Outline each blood parasite and name the species.
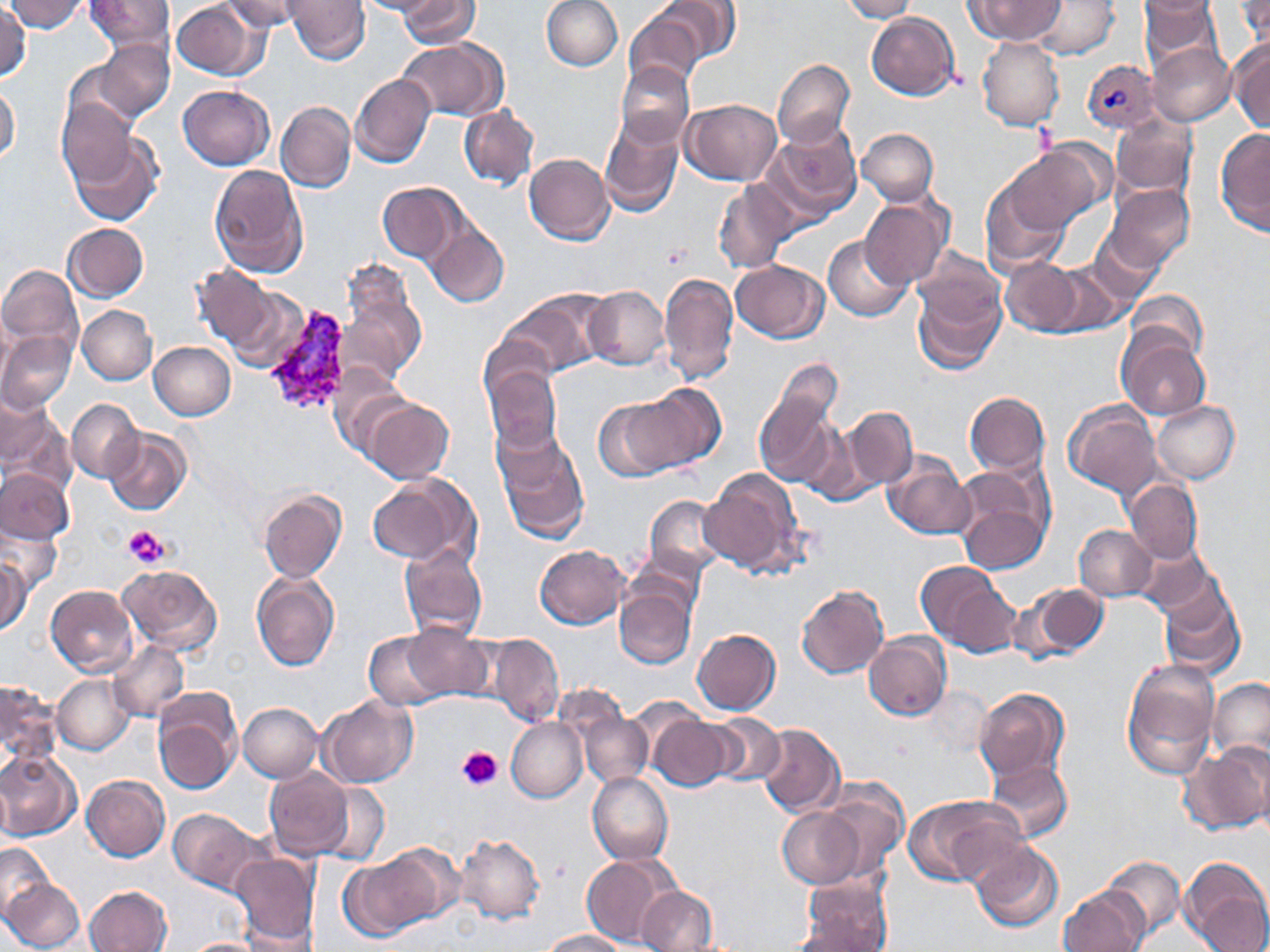
Approximate bounding boxes as named x1/y1/x2/y2 corners in pixels.
Plasmodium vivax-infected red blood cells: (x1=1082, y1=59, x2=1161, y2=133), (x1=261, y1=302, x2=355, y2=417).
No Plasmodium falciparum, Plasmodium ovale, Plasmodium malariae, Babesia divergens, or Trypanosoma brucei observed.

Summary:
  - Uninfected red blood cell locations: (x1=5, y1=0, x2=88, y2=32), (x1=86, y1=0, x2=173, y2=55), (x1=220, y1=0, x2=303, y2=32), (x1=285, y1=0, x2=370, y2=64), (x1=356, y1=0, x2=449, y2=18), (x1=399, y1=0, x2=478, y2=47), (x1=541, y1=0, x2=621, y2=70), (x1=655, y1=0, x2=739, y2=65), (x1=840, y1=0, x2=917, y2=22), (x1=966, y1=0, x2=1066, y2=45), (x1=1028, y1=0, x2=1119, y2=60), (x1=1139, y1=0, x2=1222, y2=71), (x1=1234, y1=0, x2=1270, y2=45), (x1=172, y1=1, x2=264, y2=79), (x1=0, y1=6, x2=30, y2=80), (x1=624, y1=11, x2=706, y2=90), (x1=866, y1=12, x2=959, y2=101), (x1=396, y1=38, x2=507, y2=120), (x1=978, y1=38, x2=1064, y2=130), (x1=92, y1=40, x2=175, y2=122), (x1=1146, y1=41, x2=1235, y2=127), (x1=1229, y1=42, x2=1270, y2=134), (x1=773, y1=59, x2=855, y2=148), (x1=61, y1=60, x2=144, y2=140), (x1=615, y1=61, x2=694, y2=151), (x1=350, y1=73, x2=435, y2=168), (x1=0, y1=82, x2=20, y2=166), (x1=179, y1=85, x2=274, y2=169), (x1=56, y1=98, x2=139, y2=186), (x1=681, y1=99, x2=782, y2=185), (x1=275, y1=101, x2=355, y2=193), (x1=458, y1=106, x2=539, y2=189), (x1=1111, y1=115, x2=1197, y2=200), (x1=598, y1=118, x2=683, y2=217), (x1=766, y1=122, x2=861, y2=218), (x1=856, y1=128, x2=939, y2=205), (x1=1216, y1=130, x2=1270, y2=235), (x1=69, y1=134, x2=162, y2=227), (x1=1005, y1=145, x2=1104, y2=233), (x1=523, y1=153, x2=614, y2=245), (x1=209, y1=163, x2=309, y2=278), (x1=980, y1=177, x2=1070, y2=271), (x1=713, y1=181, x2=797, y2=272), (x1=377, y1=183, x2=465, y2=263), (x1=1105, y1=184, x2=1194, y2=273), (x1=860, y1=197, x2=949, y2=289), (x1=423, y1=221, x2=509, y2=308), (x1=62, y1=223, x2=148, y2=301), (x1=1087, y1=228, x2=1163, y2=305), (x1=824, y1=235, x2=913, y2=321), (x1=911, y1=248, x2=1006, y2=326), (x1=999, y1=258, x2=1081, y2=335), (x1=1047, y1=260, x2=1128, y2=336), (x1=731, y1=261, x2=827, y2=342), (x1=0, y1=263, x2=83, y2=355), (x1=190, y1=265, x2=276, y2=349), (x1=659, y1=272, x2=738, y2=384), (x1=912, y1=274, x2=1006, y2=376), (x1=339, y1=283, x2=427, y2=384), (x1=583, y1=286, x2=670, y2=370), (x1=228, y1=287, x2=308, y2=372), (x1=501, y1=290, x2=602, y2=378), (x1=1127, y1=290, x2=1207, y2=362), (x1=77, y1=305, x2=157, y2=385), (x1=0, y1=319, x2=10, y2=391), (x1=1118, y1=331, x2=1211, y2=421), (x1=0, y1=333, x2=76, y2=413), (x1=148, y1=341, x2=236, y2=421), (x1=766, y1=359, x2=844, y2=445), (x1=328, y1=364, x2=414, y2=458), (x1=483, y1=364, x2=563, y2=455), (x1=755, y1=382, x2=841, y2=487), (x1=632, y1=384, x2=725, y2=469), (x1=964, y1=391, x2=1049, y2=477), (x1=1, y1=394, x2=53, y2=468), (x1=594, y1=397, x2=691, y2=481), (x1=67, y1=399, x2=143, y2=482), (x1=364, y1=399, x2=454, y2=484), (x1=1152, y1=400, x2=1240, y2=484), (x1=1064, y1=401, x2=1162, y2=497), (x1=840, y1=406, x2=918, y2=491), (x1=103, y1=429, x2=191, y2=516), (x1=494, y1=431, x2=589, y2=543), (x1=883, y1=456, x2=976, y2=539), (x1=951, y1=465, x2=1053, y2=570), (x1=0, y1=468, x2=73, y2=544), (x1=698, y1=469, x2=806, y2=576), (x1=368, y1=474, x2=473, y2=566), (x1=1124, y1=478, x2=1203, y2=565), (x1=259, y1=490, x2=347, y2=583), (x1=644, y1=496, x2=727, y2=577), (x1=1074, y1=524, x2=1158, y2=601), (x1=2, y1=525, x2=62, y2=595), (x1=1134, y1=541, x2=1218, y2=619), (x1=397, y1=543, x2=486, y2=641), (x1=534, y1=545, x2=629, y2=630), (x1=1, y1=556, x2=30, y2=635), (x1=915, y1=561, x2=1014, y2=655), (x1=117, y1=564, x2=221, y2=655), (x1=251, y1=573, x2=340, y2=673), (x1=1158, y1=581, x2=1246, y2=679), (x1=1029, y1=584, x2=1110, y2=660), (x1=45, y1=585, x2=137, y2=678), (x1=614, y1=585, x2=696, y2=670), (x1=796, y1=585, x2=889, y2=679), (x1=400, y1=626, x2=492, y2=702), (x1=693, y1=628, x2=781, y2=716), (x1=363, y1=630, x2=446, y2=709), (x1=486, y1=633, x2=563, y2=725), (x1=864, y1=633, x2=951, y2=721), (x1=107, y1=641, x2=189, y2=722), (x1=1121, y1=659, x2=1219, y2=777), (x1=53, y1=674, x2=134, y2=754), (x1=1208, y1=678, x2=1270, y2=766), (x1=1, y1=680, x2=60, y2=767), (x1=974, y1=687, x2=1071, y2=786), (x1=152, y1=691, x2=241, y2=795), (x1=317, y1=696, x2=417, y2=788), (x1=238, y1=703, x2=323, y2=782), (x1=704, y1=711, x2=785, y2=788), (x1=581, y1=712, x2=653, y2=786), (x1=648, y1=716, x2=735, y2=791), (x1=506, y1=717, x2=587, y2=802), (x1=756, y1=723, x2=846, y2=817), (x1=1184, y1=741, x2=1270, y2=835), (x1=0, y1=751, x2=81, y2=840), (x1=984, y1=758, x2=1072, y2=844), (x1=264, y1=769, x2=352, y2=860), (x1=587, y1=772, x2=673, y2=865), (x1=0, y1=774, x2=12, y2=848), (x1=82, y1=776, x2=170, y2=861), (x1=816, y1=779, x2=909, y2=877), (x1=315, y1=785, x2=389, y2=866), (x1=905, y1=794, x2=1023, y2=887), (x1=777, y1=806, x2=864, y2=888), (x1=167, y1=808, x2=267, y2=894), (x1=454, y1=833, x2=546, y2=925), (x1=968, y1=839, x2=1063, y2=931), (x1=0, y1=842, x2=55, y2=917), (x1=374, y1=844, x2=465, y2=926), (x1=230, y1=854, x2=320, y2=947), (x1=341, y1=854, x2=441, y2=940), (x1=579, y1=854, x2=678, y2=949), (x1=1100, y1=855, x2=1187, y2=939), (x1=1179, y1=856, x2=1270, y2=952), (x1=798, y1=874, x2=893, y2=951), (x1=2, y1=878, x2=84, y2=951), (x1=85, y1=886, x2=172, y2=952), (x1=635, y1=886, x2=718, y2=952), (x1=1059, y1=886, x2=1150, y2=952), (x1=786, y1=920, x2=883, y2=951), (x1=539, y1=929, x2=628, y2=951), (x1=180, y1=937, x2=269, y2=952)
  - Platelet locations: (x1=122, y1=525, x2=167, y2=567), (x1=457, y1=745, x2=503, y2=790)
  - Slide-level diagnosis: Plasmodium vivax
  - Modality: light microscopy
  - Preparation: thin blood smear
  - Stain: May-Grünwald-Giemsa
  - Field of view: one of a larger specimen
  - Magnification: 1000x
  - Image size: 1270×952 pixels